State which parasite is depicted.
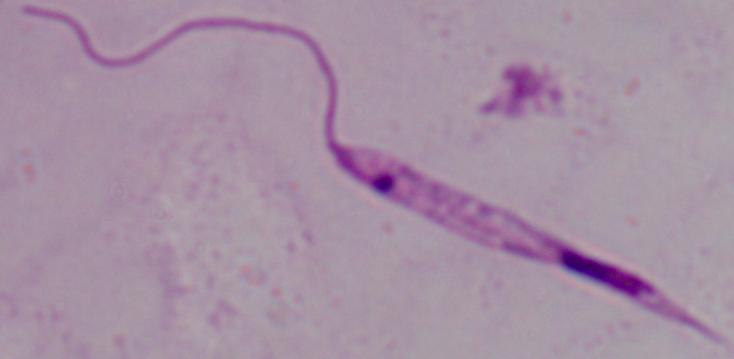

This is Leishmania.

Captured at 1000x magnification. Micrograph.